Describe the morphology of the erythrocytes.
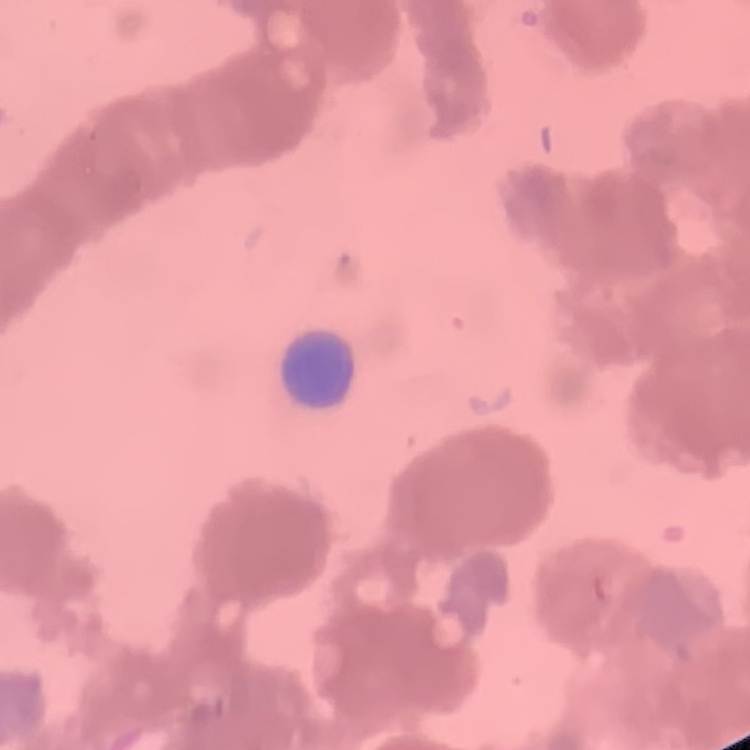

They show rouleaux formation.

image type = one tile cut from a larger photomicrograph
stain = Field's or Giemsa
preparation = thin blood film